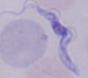

Photomicrograph. A trypanosome is shown. Captured at 1000x magnification.